Point out each malaria parasite.
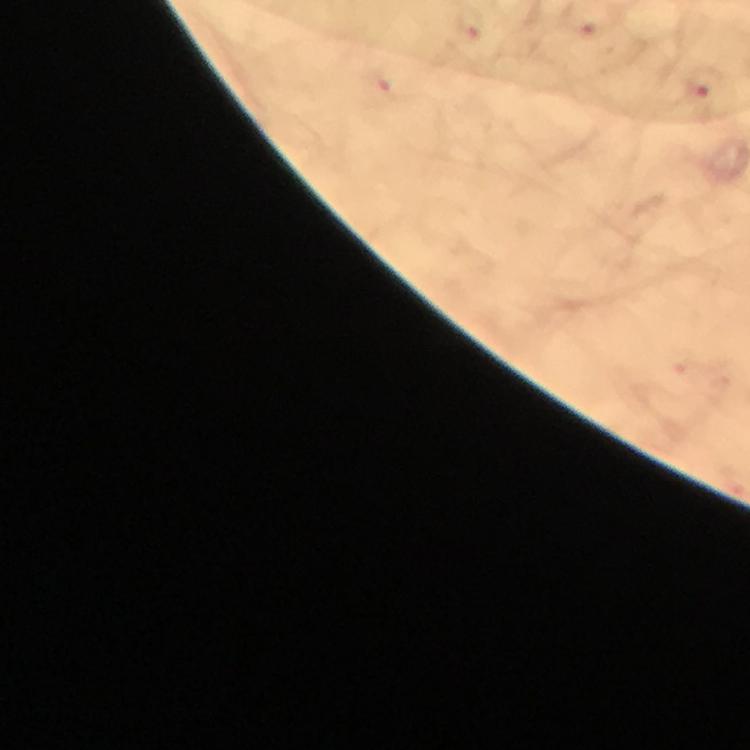

Approximate object centers, in pixels from the top-left corner.
Malaria parasites: (x=471, y=28), (x=389, y=83), (x=699, y=85).

Summary:
  - Preparation: thick smear
  - Magnification: 100x
  - Cropped from: one field of view
  - Stain: Giemsa
  - Capture: smartphone mounted on the microscope
  - Image size: 750×750 pixels
  - Immersion oil: used
  - Context: from a diagnostic examination for malaria